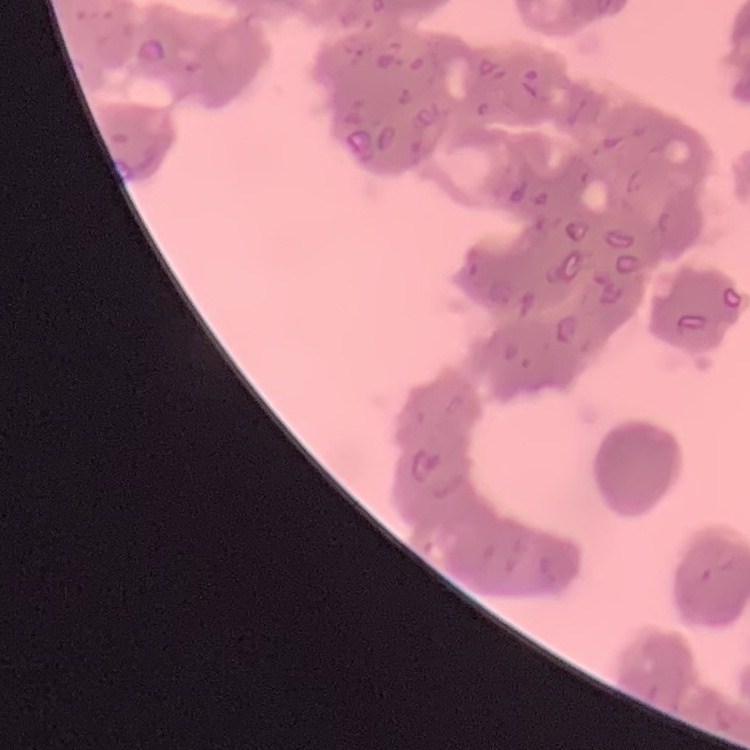

{
  "erythrocyte_morphology": "rouleaux formation",
  "image_type": "one tile cut from a larger photomicrograph",
  "stain": "Field's or Giemsa",
  "preparation": "thin blood smear"
}